Assess this cell for malaria.
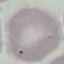

Uninfected.

Summary:
  - Preparation: thin blood smear
  - Stain: Giemsa
  - Capture: smartphone camera at the microscope eyepiece
  - Image type: cell patch, automatically extracted from a larger field of view and resized to 64 × 64 pixels